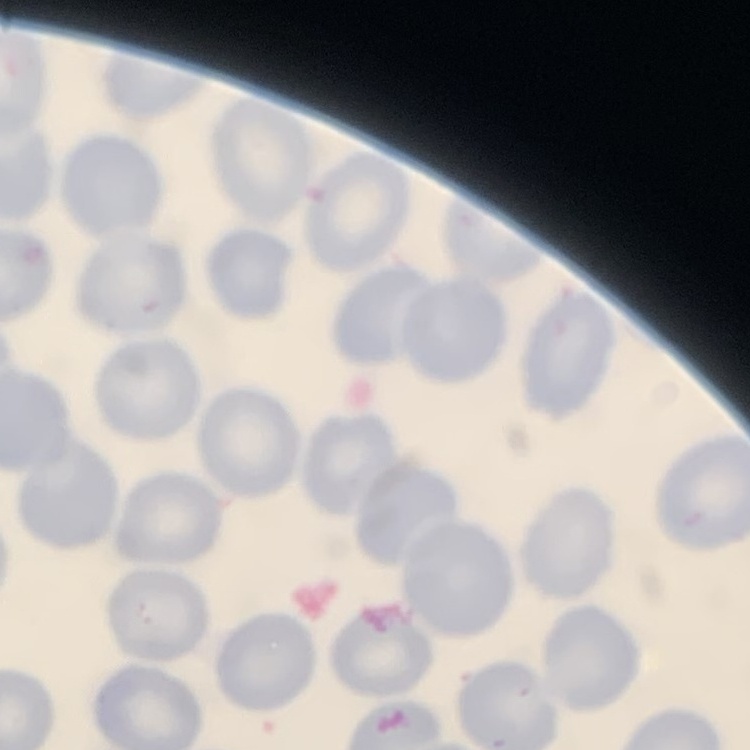
red_blood_cell_morphology: no rouleaux formation
image_type: square crop of a larger photomicrograph
stain: Field's or Giemsa
preparation: thin peripheral smear